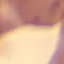

Summary:
  - Malaria status: uninfected
  - Preparation: thin blood film
  - Image type: automatically extracted cell patch, resized to 64 × 64 pixels
  - Capture: smartphone through the microscope eyepiece
  - Stain: Giemsa